Report the malaria status of this cell.
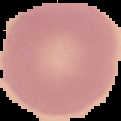

It is uninfected.

Segmented cell region on a black background. Image is 121×121 pixels. From a thin blood film.